Report the malaria status of this cell.
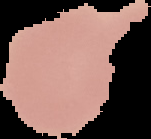

Uninfected.

Image is 151×139 pixels. The area outside the segmented cell region is set to black. From a thin blood film.